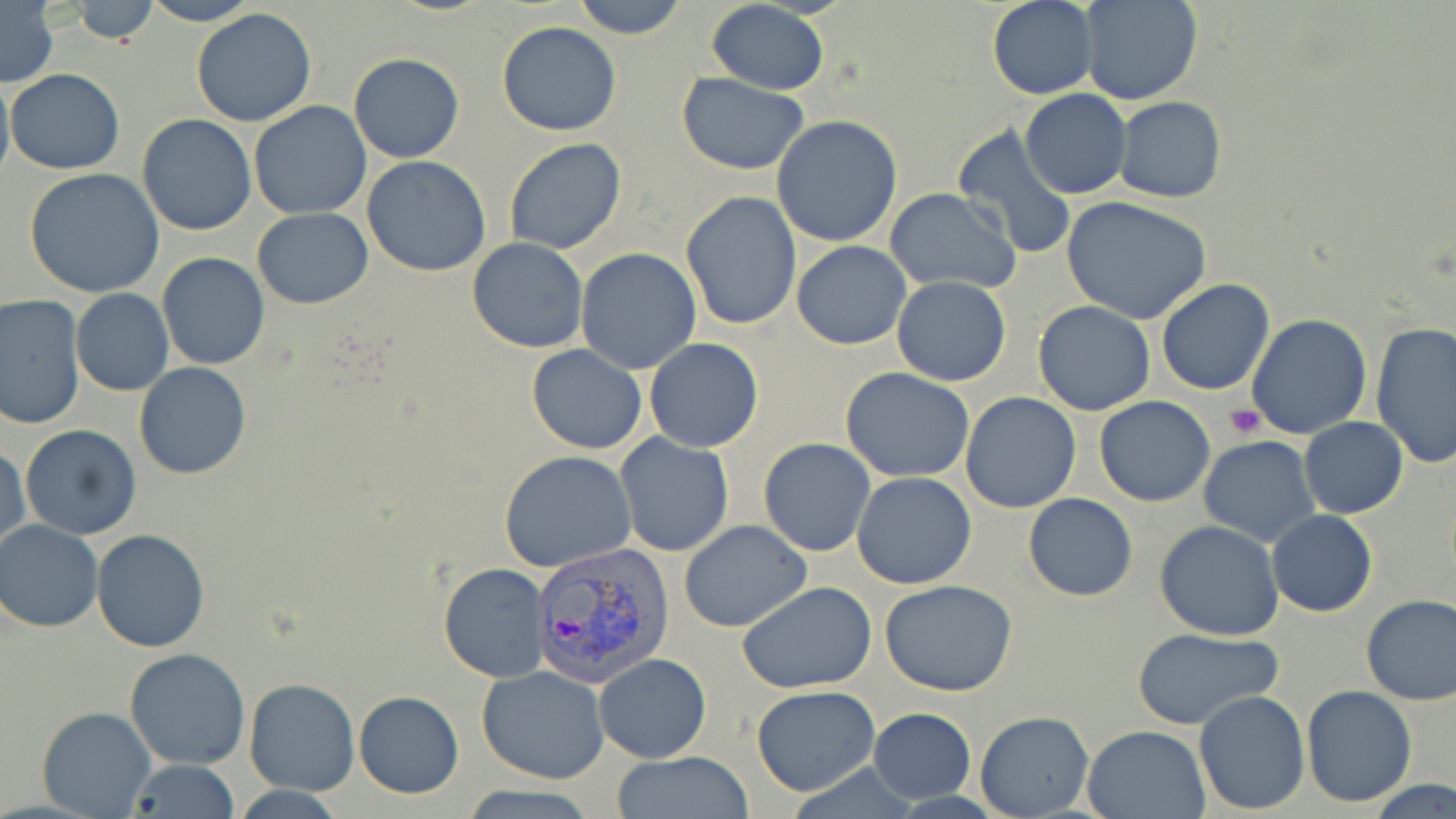

Summary:
  - Coordinate format: approximate bounding boxes as named x1/y1/x2/y2 corners in pixels
  - Platelet locations: (x1=1226, y1=406, x2=1265, y2=439)
  - Uninfected red blood cell locations: (x1=67, y1=0, x2=158, y2=46), (x1=570, y1=0, x2=688, y2=40), (x1=1080, y1=0, x2=1201, y2=106), (x1=138, y1=1, x2=260, y2=25), (x1=706, y1=1, x2=829, y2=95), (x1=987, y1=1, x2=1098, y2=100), (x1=1, y1=3, x2=59, y2=89), (x1=190, y1=8, x2=318, y2=127), (x1=496, y1=21, x2=621, y2=136), (x1=349, y1=53, x2=465, y2=163), (x1=7, y1=68, x2=125, y2=176), (x1=0, y1=69, x2=14, y2=192), (x1=677, y1=73, x2=807, y2=175), (x1=1020, y1=88, x2=1132, y2=199), (x1=1113, y1=96, x2=1226, y2=203), (x1=248, y1=101, x2=374, y2=220), (x1=136, y1=114, x2=257, y2=236), (x1=771, y1=116, x2=904, y2=248), (x1=952, y1=124, x2=1079, y2=261), (x1=504, y1=138, x2=629, y2=255), (x1=361, y1=156, x2=491, y2=277), (x1=24, y1=167, x2=167, y2=299), (x1=886, y1=188, x2=1023, y2=293), (x1=679, y1=190, x2=802, y2=330), (x1=1062, y1=195, x2=1213, y2=323), (x1=252, y1=208, x2=374, y2=309), (x1=466, y1=238, x2=591, y2=353), (x1=792, y1=240, x2=911, y2=349), (x1=576, y1=247, x2=703, y2=374), (x1=157, y1=253, x2=270, y2=370), (x1=892, y1=276, x2=1011, y2=387), (x1=1156, y1=279, x2=1274, y2=394), (x1=71, y1=288, x2=174, y2=396), (x1=0, y1=294, x2=85, y2=430), (x1=1033, y1=301, x2=1157, y2=416), (x1=1246, y1=313, x2=1373, y2=440), (x1=1370, y1=321, x2=1456, y2=468), (x1=643, y1=338, x2=764, y2=452), (x1=527, y1=344, x2=648, y2=454), (x1=134, y1=362, x2=252, y2=479), (x1=840, y1=367, x2=976, y2=483), (x1=959, y1=391, x2=1081, y2=513), (x1=795, y1=395, x2=947, y2=536), (x1=1095, y1=396, x2=1216, y2=506), (x1=1299, y1=417, x2=1408, y2=518), (x1=19, y1=424, x2=143, y2=541), (x1=614, y1=432, x2=736, y2=557), (x1=1199, y1=436, x2=1320, y2=546), (x1=759, y1=437, x2=876, y2=557), (x1=1, y1=441, x2=28, y2=553), (x1=500, y1=450, x2=637, y2=574), (x1=851, y1=473, x2=977, y2=589), (x1=1023, y1=492, x2=1137, y2=603), (x1=1266, y1=510, x2=1378, y2=618), (x1=0, y1=520, x2=103, y2=632), (x1=1155, y1=520, x2=1285, y2=640), (x1=678, y1=521, x2=810, y2=632), (x1=92, y1=529, x2=210, y2=651), (x1=437, y1=564, x2=552, y2=683), (x1=879, y1=580, x2=1020, y2=696), (x1=737, y1=581, x2=877, y2=694), (x1=1359, y1=595, x2=1456, y2=706), (x1=1129, y1=625, x2=1283, y2=730), (x1=124, y1=647, x2=251, y2=770), (x1=593, y1=653, x2=712, y2=763), (x1=477, y1=666, x2=609, y2=784), (x1=244, y1=679, x2=360, y2=796), (x1=751, y1=684, x2=880, y2=797), (x1=1300, y1=685, x2=1417, y2=807), (x1=353, y1=689, x2=464, y2=799), (x1=1194, y1=691, x2=1310, y2=812), (x1=36, y1=707, x2=155, y2=818), (x1=869, y1=707, x2=976, y2=802), (x1=975, y1=710, x2=1092, y2=819), (x1=1082, y1=726, x2=1210, y2=817), (x1=610, y1=753, x2=758, y2=817), (x1=128, y1=759, x2=239, y2=819), (x1=1368, y1=779, x2=1456, y2=818), (x1=458, y1=784, x2=601, y2=818)
  - Plasmodium vivax-infected red blood cell locations: (x1=529, y1=540, x2=676, y2=685)
  - Slide-level diagnosis: Plasmodium vivax
  - Stain: May-Grünwald-Giemsa
  - Magnification: 1000x
  - Preparation: thin blood smear
  - Field of view: one of a larger specimen
  - Image size: 1456×819 pixels
  - Modality: optical microscopy